Name the blood parasite species.
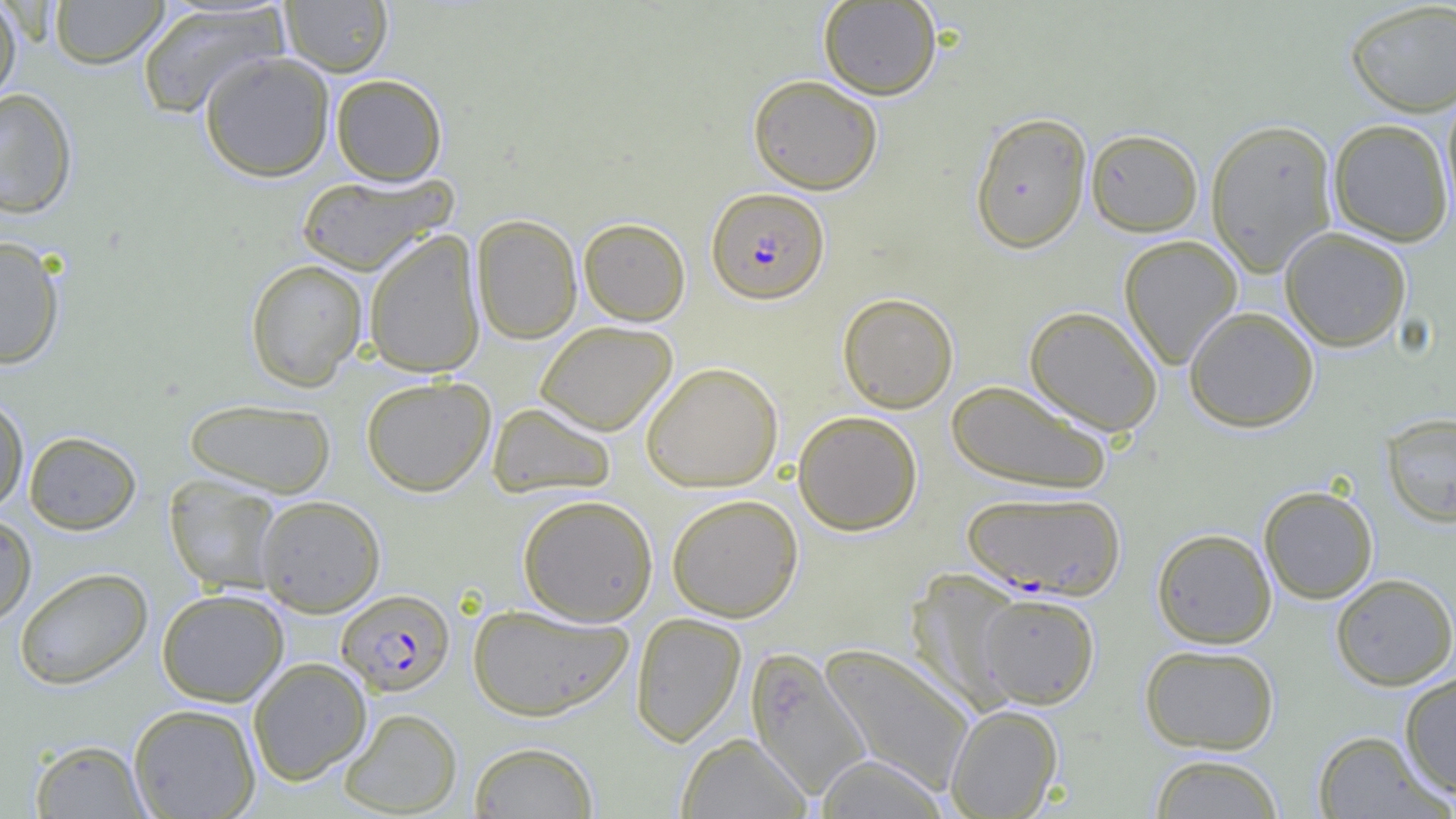
Plasmodium falciparum.

Summary:
  - Coordinate format: approximate bounding boxes as named x1/y1/x2/y2 corners in pixels
  - Uninfected red blood cell locations: (x1=49, y1=0, x2=169, y2=69), (x1=0, y1=1, x2=23, y2=105), (x1=280, y1=1, x2=394, y2=76), (x1=818, y1=1, x2=942, y2=100), (x1=1344, y1=1, x2=1456, y2=117), (x1=136, y1=3, x2=288, y2=120), (x1=199, y1=50, x2=335, y2=182), (x1=331, y1=74, x2=447, y2=185), (x1=747, y1=74, x2=883, y2=194), (x1=1440, y1=85, x2=1456, y2=230), (x1=0, y1=88, x2=78, y2=218), (x1=969, y1=111, x2=1092, y2=254), (x1=1205, y1=118, x2=1339, y2=276), (x1=1328, y1=118, x2=1454, y2=247), (x1=1086, y1=128, x2=1204, y2=236), (x1=295, y1=171, x2=457, y2=275), (x1=471, y1=214, x2=583, y2=345), (x1=578, y1=217, x2=691, y2=325), (x1=1279, y1=227, x2=1412, y2=352), (x1=363, y1=229, x2=486, y2=378), (x1=1119, y1=235, x2=1243, y2=370), (x1=0, y1=236, x2=66, y2=369), (x1=245, y1=259, x2=368, y2=392), (x1=837, y1=292, x2=959, y2=413), (x1=1024, y1=305, x2=1163, y2=436), (x1=1184, y1=306, x2=1320, y2=432), (x1=535, y1=320, x2=677, y2=436), (x1=640, y1=361, x2=784, y2=492), (x1=360, y1=376, x2=495, y2=496), (x1=945, y1=380, x2=1112, y2=495), (x1=0, y1=396, x2=29, y2=513), (x1=183, y1=398, x2=336, y2=498), (x1=487, y1=402, x2=617, y2=499), (x1=792, y1=410, x2=923, y2=535), (x1=1381, y1=412, x2=1456, y2=528), (x1=24, y1=430, x2=141, y2=535), (x1=164, y1=474, x2=284, y2=596), (x1=1258, y1=485, x2=1378, y2=604), (x1=517, y1=493, x2=659, y2=626), (x1=667, y1=493, x2=803, y2=622), (x1=256, y1=495, x2=386, y2=616), (x1=0, y1=514, x2=37, y2=627), (x1=1151, y1=527, x2=1277, y2=648), (x1=14, y1=567, x2=153, y2=690), (x1=906, y1=570, x2=1029, y2=713), (x1=1330, y1=573, x2=1456, y2=690), (x1=157, y1=589, x2=289, y2=706), (x1=978, y1=593, x2=1100, y2=708), (x1=468, y1=603, x2=633, y2=721), (x1=630, y1=612, x2=747, y2=747), (x1=818, y1=642, x2=975, y2=795), (x1=1139, y1=644, x2=1279, y2=754), (x1=745, y1=647, x2=872, y2=800), (x1=248, y1=657, x2=372, y2=786), (x1=1399, y1=670, x2=1456, y2=798), (x1=129, y1=703, x2=261, y2=819), (x1=945, y1=704, x2=1064, y2=818), (x1=339, y1=707, x2=462, y2=817), (x1=1312, y1=730, x2=1451, y2=818), (x1=676, y1=732, x2=812, y2=819), (x1=29, y1=739, x2=151, y2=818), (x1=468, y1=741, x2=599, y2=818), (x1=1148, y1=753, x2=1285, y2=819), (x1=815, y1=754, x2=951, y2=818)
  - Plasmodium falciparum-infected red blood cell locations: (x1=706, y1=187, x2=830, y2=304), (x1=963, y1=490, x2=1125, y2=600), (x1=337, y1=589, x2=455, y2=696)
  - Field of view: one of a larger specimen
  - Modality: light microscopy
  - Image size: 1456×819 pixels
  - Preparation: thin blood smear
  - Magnification: 1000x